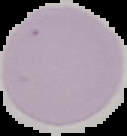
Summary:
  - Image type: segmented cell region with the area outside set to black
  - Preparation: thin blood film
  - Image size: 127×136 pixels
  - Result: no malaria parasites detected